Name the parasite shown.
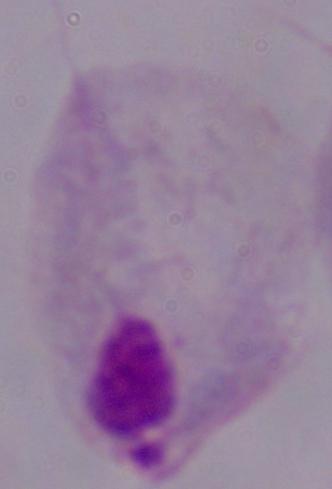
This is a trichomonad.

Micrograph. 1000x magnification.